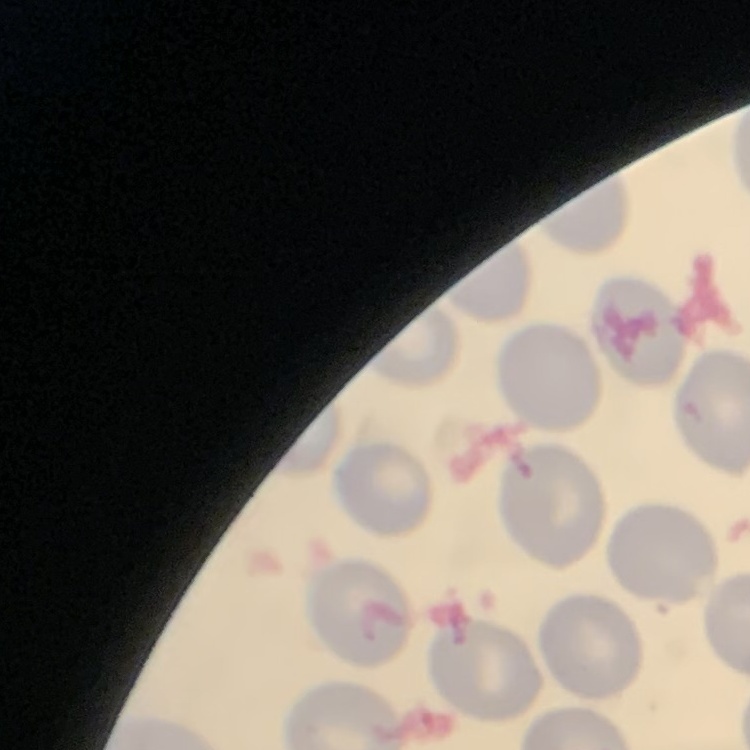
Summary:
  - Erythrocyte morphology: no rouleaux formation
  - Preparation: thin peripheral smear
  - Stain: Field's or Giemsa
  - Image type: one tile cut from a larger photomicrograph